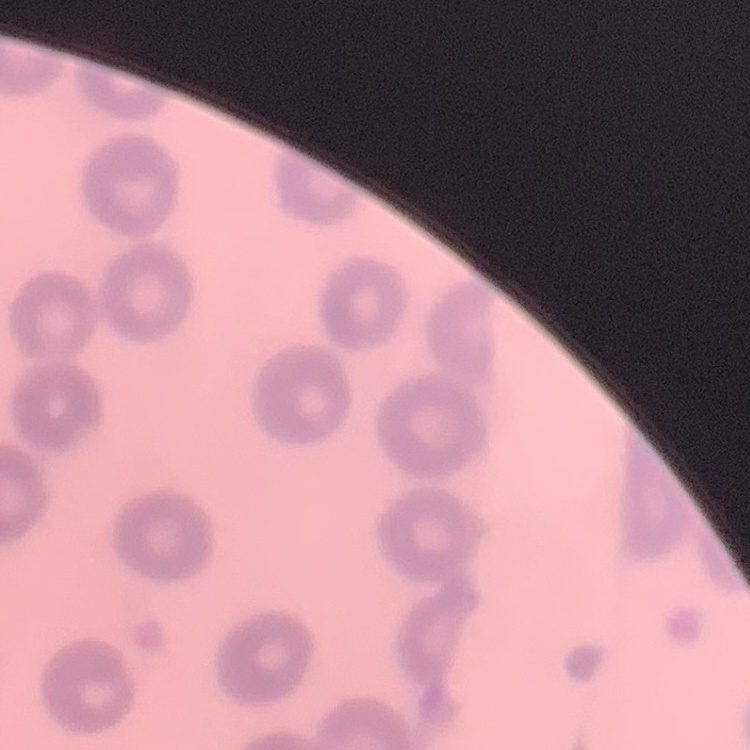

Summary:
  - Red blood cell morphology: no rouleaux formation
  - Preparation: thin blood film
  - Stain: Field's or Giemsa
  - Image type: one tile cut from a larger photomicrograph